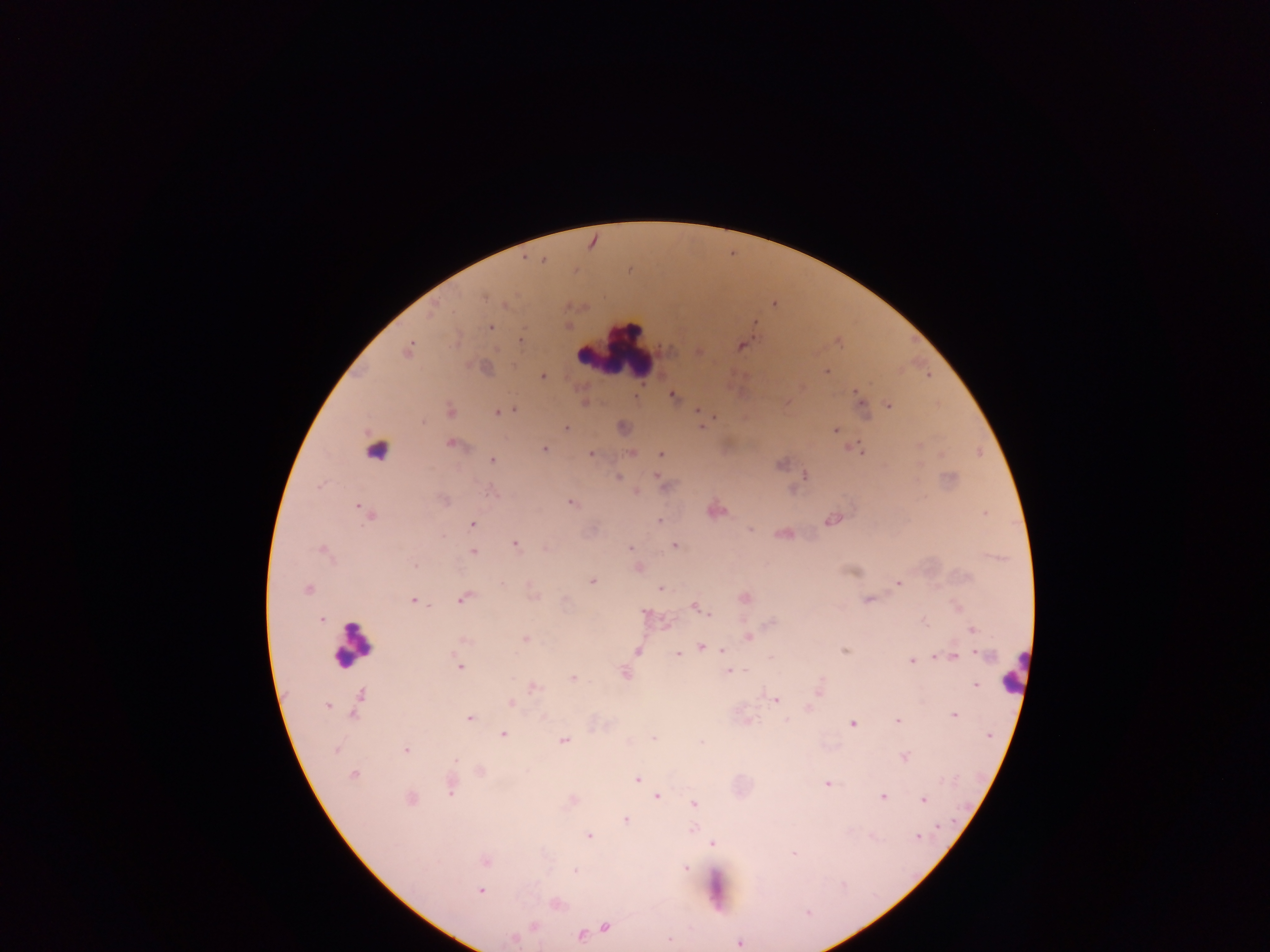

country = Ghana
leukocyte locations = approximate centers as (x, y) in pixels: (615, 350), (378, 446), (351, 643), (1013, 671)
preparation = thick blood film
malaria parasite locations = approximate centers as (x, y) in pixels: (542, 261), (485, 297), (491, 327), (520, 340), (741, 346), (409, 349), (826, 372), (543, 376), (857, 394), (673, 396), (860, 402), (889, 405), (514, 410), (697, 410), (450, 411), (497, 412), (714, 418), (423, 422), (703, 427), (566, 428), (835, 430), (450, 443), (860, 449), (545, 450), (591, 453), (632, 454), (661, 454), (492, 460), (805, 475), (656, 476), (619, 477), (637, 492), (570, 502), (359, 508), (368, 514), (985, 514), (832, 520), (659, 521), (472, 524), (749, 530), (441, 537), (515, 544), (674, 545), (545, 548), (631, 548), (321, 549), (474, 552), (415, 565), (592, 581), (898, 583), (307, 589), (660, 589), (464, 599), (868, 600), (414, 601), (697, 607), (644, 612), (709, 613), (321, 619), (926, 623), (972, 629), (748, 636), (525, 638), (465, 641), (700, 647), (722, 651), (845, 651), (638, 652), (677, 654), (985, 655), (771, 657), (954, 657), (934, 658), (912, 661), (460, 667), (729, 671), (624, 673), (573, 678), (975, 684), (534, 688), (361, 694), (775, 699), (511, 703), (327, 706), (353, 714), (954, 715), (469, 719), (898, 720), (852, 724), (503, 734), (652, 738), (564, 741), (336, 750), (406, 750), (904, 756), (454, 761), (480, 771), (353, 775), (637, 779), (827, 784), (451, 789), (657, 796), (883, 796), (411, 798), (923, 800), (695, 804), (625, 819), (939, 826), (693, 828), (589, 836), (917, 836), (713, 843), (793, 854), (485, 861), (685, 868), (575, 871), (481, 891), (808, 912), (534, 927), (605, 927), (581, 936), (513, 939), (669, 939), (739, 943)
image size = 1270×952 pixels
field of view = single
capture = mobile-phone photograph through a microscope